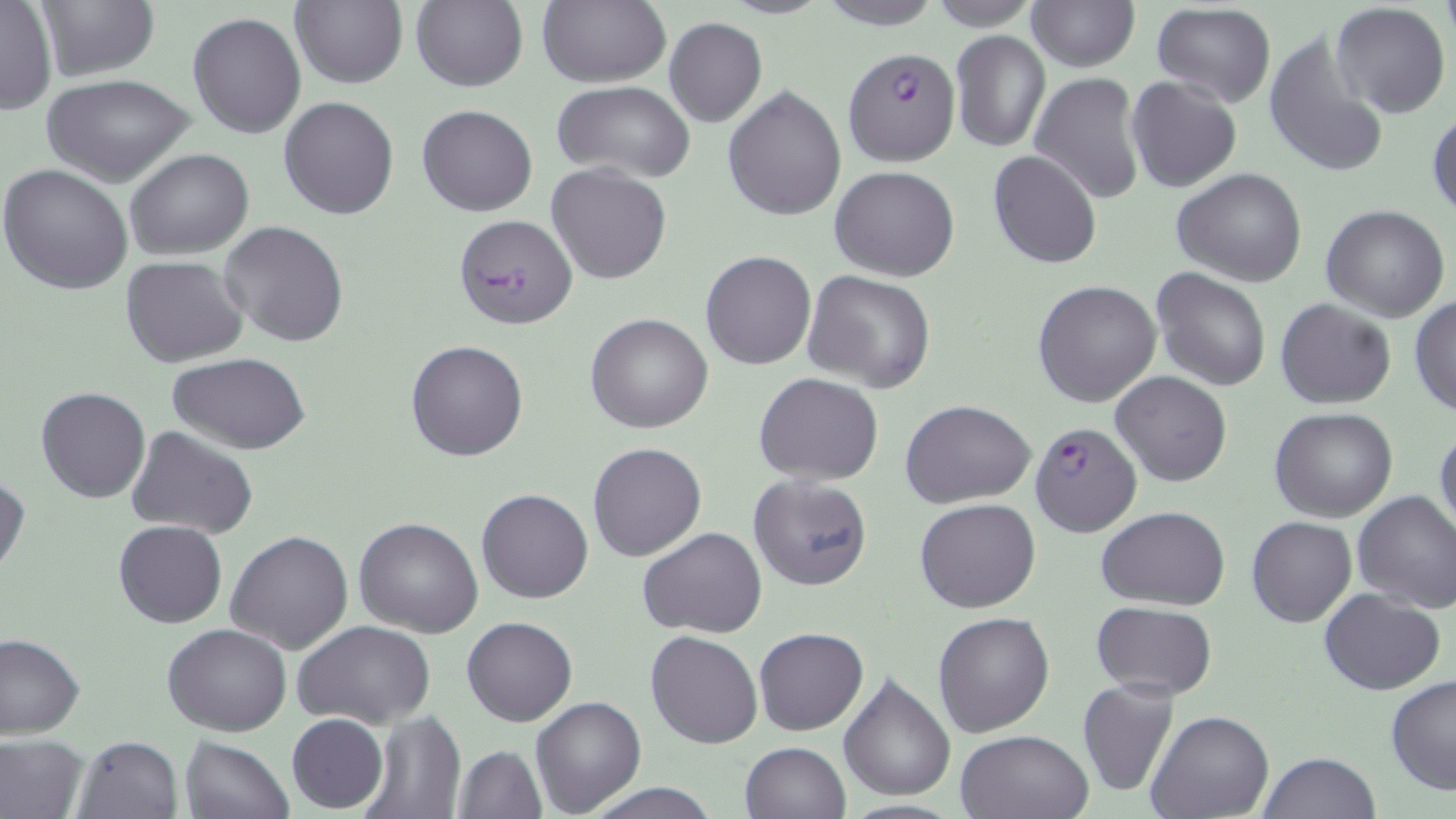

Approximate bounding boxes as named x1/y1/x2/y2 corners in pixels. Uninfected red blood cell locations: (x1=410, y1=0, x2=529, y2=93), (x1=814, y1=0, x2=944, y2=30), (x1=1, y1=1, x2=56, y2=114), (x1=288, y1=1, x2=408, y2=89), (x1=536, y1=1, x2=671, y2=88), (x1=923, y1=1, x2=1043, y2=30), (x1=1027, y1=1, x2=1138, y2=71), (x1=30, y1=3, x2=157, y2=81), (x1=1332, y1=3, x2=1450, y2=118), (x1=1151, y1=4, x2=1276, y2=109), (x1=187, y1=11, x2=305, y2=139), (x1=663, y1=16, x2=767, y2=127), (x1=949, y1=30, x2=1052, y2=152), (x1=1263, y1=31, x2=1391, y2=179), (x1=687, y1=50, x2=811, y2=202), (x1=1029, y1=72, x2=1146, y2=204), (x1=42, y1=73, x2=195, y2=187), (x1=1125, y1=76, x2=1243, y2=194), (x1=553, y1=81, x2=699, y2=182), (x1=723, y1=86, x2=847, y2=221), (x1=278, y1=96, x2=400, y2=220), (x1=417, y1=103, x2=538, y2=216), (x1=1427, y1=108, x2=1456, y2=222), (x1=124, y1=147, x2=255, y2=260), (x1=989, y1=149, x2=1102, y2=268), (x1=548, y1=163, x2=672, y2=284), (x1=0, y1=164, x2=133, y2=296), (x1=830, y1=165, x2=959, y2=281), (x1=1171, y1=168, x2=1308, y2=288), (x1=1320, y1=204, x2=1450, y2=322), (x1=453, y1=214, x2=577, y2=327), (x1=217, y1=221, x2=350, y2=350), (x1=700, y1=250, x2=817, y2=370), (x1=122, y1=256, x2=247, y2=368), (x1=1151, y1=267, x2=1271, y2=391), (x1=802, y1=270, x2=937, y2=393), (x1=1032, y1=279, x2=1162, y2=408), (x1=1408, y1=295, x2=1456, y2=416), (x1=1274, y1=297, x2=1396, y2=409), (x1=586, y1=312, x2=713, y2=434), (x1=406, y1=339, x2=529, y2=462), (x1=168, y1=352, x2=311, y2=454), (x1=1109, y1=370, x2=1232, y2=488), (x1=755, y1=372, x2=884, y2=486), (x1=35, y1=387, x2=151, y2=503), (x1=901, y1=398, x2=1037, y2=506), (x1=1269, y1=407, x2=1398, y2=522), (x1=1434, y1=423, x2=1456, y2=539), (x1=125, y1=425, x2=260, y2=541), (x1=588, y1=442, x2=707, y2=562), (x1=0, y1=471, x2=28, y2=583), (x1=748, y1=474, x2=873, y2=590), (x1=476, y1=487, x2=593, y2=603), (x1=1352, y1=490, x2=1456, y2=612), (x1=914, y1=498, x2=1041, y2=613), (x1=1097, y1=505, x2=1230, y2=608), (x1=1247, y1=515, x2=1356, y2=627), (x1=354, y1=516, x2=484, y2=638), (x1=113, y1=520, x2=227, y2=629), (x1=638, y1=526, x2=769, y2=638), (x1=225, y1=529, x2=354, y2=654), (x1=1318, y1=588, x2=1446, y2=695), (x1=1090, y1=600, x2=1217, y2=701), (x1=932, y1=611, x2=1054, y2=738), (x1=461, y1=614, x2=578, y2=726), (x1=293, y1=621, x2=438, y2=732), (x1=162, y1=622, x2=292, y2=735), (x1=753, y1=627, x2=868, y2=735), (x1=646, y1=631, x2=762, y2=749), (x1=0, y1=633, x2=87, y2=739), (x1=838, y1=672, x2=956, y2=802), (x1=1386, y1=675, x2=1456, y2=794), (x1=1077, y1=678, x2=1181, y2=800), (x1=530, y1=696, x2=646, y2=817), (x1=1145, y1=709, x2=1275, y2=819), (x1=361, y1=710, x2=466, y2=819), (x1=286, y1=712, x2=389, y2=812), (x1=956, y1=727, x2=1093, y2=819), (x1=71, y1=733, x2=183, y2=819), (x1=0, y1=734, x2=89, y2=819), (x1=181, y1=736, x2=294, y2=819), (x1=739, y1=741, x2=851, y2=819), (x1=453, y1=743, x2=547, y2=817), (x1=1258, y1=750, x2=1381, y2=818), (x1=581, y1=779, x2=723, y2=818). Plasmodium falciparum-infected red blood cell locations: (x1=843, y1=44, x2=959, y2=166), (x1=1029, y1=420, x2=1141, y2=538). Slide-level diagnosis: Plasmodium falciparum. May-Grünwald-Giemsa-stained preparation. Light microscopy. Thin blood smear. One field of a larger specimen. 1000x magnification. Image is 1456×819 pixels.